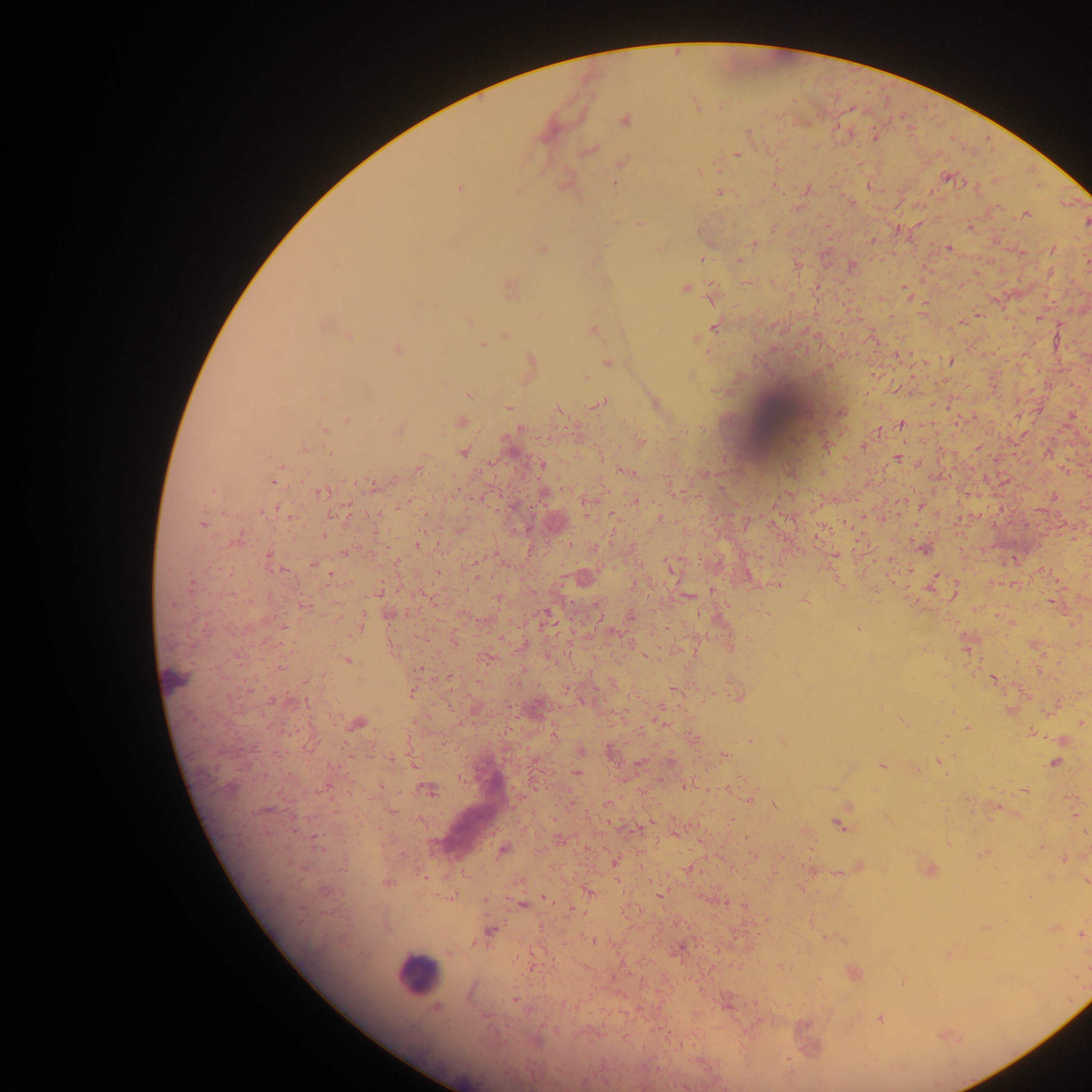
Approximate centers as x y in pixels.
Summary:
  - Plasmodium parasite locations: 696 105; 624 119; 747 131; 874 135; 588 150; 737 154; 622 160; 698 172; 947 177; 615 182; 868 185; 458 188; 807 189; 719 192; 1025 214; 616 222; 640 224; 969 227; 872 241; 753 243; 948 247; 541 249; 1052 249; 702 258; 738 260; 1087 263; 797 264; 850 265; 1049 272; 746 282; 959 285; 510 286; 685 288; 905 290; 711 295; 978 315; 467 322; 959 323; 321 324; 715 326; 592 330; 348 336; 505 336; 696 338; 482 344; 397 349; 898 354; 951 361; 531 363; 607 363; 828 364; 873 374; 584 377; 898 389; 469 393; 322 397; 599 402; 654 403; 508 407; 557 409; 841 411; 1071 416; 347 420; 460 422; 901 424; 323 429; 398 431; 878 431; 639 441; 827 446; 863 446; 977 447; 463 451; 897 459; 542 465; 418 467; 624 470; 273 480; 373 486; 320 492; 966 495; 483 496; 1053 496; 587 500; 636 501; 403 504; 920 506; 611 515; 659 518; 882 519; 202 523; 555 523; 324 536; 817 537; 236 541; 418 545; 924 548; 835 555; 269 556; 890 558; 313 563; 671 567; 583 578; 837 578; 934 581; 776 583; 633 585; 1013 585; 712 590; 955 591; 379 593; 687 596; 499 598; 805 599; 1052 602; 302 605; 388 614; 547 614; 629 618; 1010 622; 361 625; 857 629; 525 644; 966 644; 730 645; 645 655; 486 657; 346 660; 1040 670; 449 677; 993 678; 674 689; 412 691; 736 694; 274 700; 1057 704; 879 706; 533 708; 1010 711; 357 722; 661 722; 906 723; 1081 723; 967 728; 1031 733; 693 738; 782 740; 750 741; 1063 741; 579 750; 611 750; 723 757; 390 758; 939 761; 1055 762; 882 765; 916 770; 576 773; 685 785; 831 788; 1025 789; 428 790; 747 798; 1071 798; 607 804; 773 804; 997 807; 392 811; 1074 814; 649 823; 839 824; 1085 832; 675 833; 314 838; 560 839; 948 843; 1041 846; 503 849; 983 853; 752 856; 1064 858; 614 862; 858 867; 689 869; 811 869; 929 870; 837 873; 1085 881; 387 883; 324 891; 588 892; 659 895; 1029 897; 544 898; 485 900; 522 904; 744 905; 767 919; 984 927; 1053 927; 490 930; 1081 933; 826 937; 593 940; 678 948; 948 954; 784 967; 852 972; 902 982; 515 999; 726 1003; 879 1019; 943 1035
  - Leukocyte locations: 779 420; 176 679; 467 821; 417 974
  - Capture: mobile-phone photograph through a microscope
  - Field of view: single
  - Preparation: thick blood film
  - Image size: 1092×1092 pixels
  - Country: Ghana